Report the malaria status of this cell.
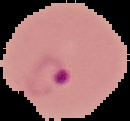
It is parasitized.

Summary:
  - Preparation: thin blood smear
  - Image type: cell region segmented out of the field of view; surrounding area masked to black
  - Image size: 130×121 pixels